Outline each Plasmodium parasite.
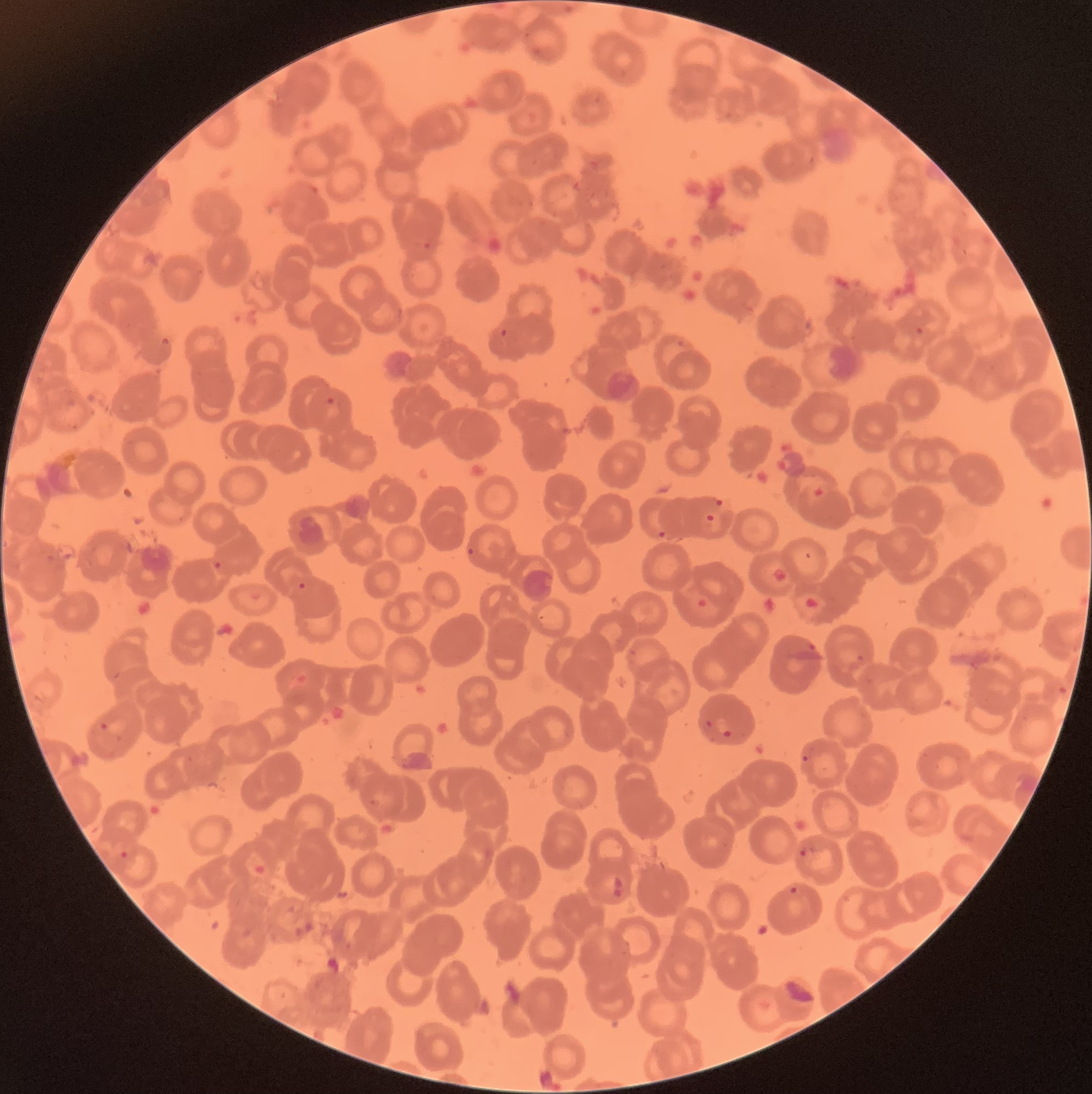
Approximate bounding boxes as [x1, y1, x2, y2] in pixels.
Plasmodium parasites: [421, 239, 435, 251], [915, 326, 924, 336], [500, 328, 507, 337], [160, 336, 172, 346], [676, 338, 685, 346], [325, 396, 335, 406], [811, 487, 826, 499], [713, 499, 726, 508], [704, 513, 717, 523], [656, 530, 667, 540], [467, 546, 477, 557], [213, 561, 222, 570], [297, 581, 307, 591], [808, 641, 817, 652], [855, 654, 865, 662], [716, 716, 732, 736], [704, 720, 714, 729], [99, 721, 109, 730], [800, 752, 810, 763], [368, 797, 383, 808], [798, 847, 813, 857], [119, 850, 130, 860], [612, 874, 625, 899], [789, 886, 802, 896], [292, 921, 316, 938].

Summary:
  - Modality: optical microscopy
  - Red blood cell morphology: rouleaux formation
  - Image size: 1092×1094 pixels
  - Preparation: thin blood film